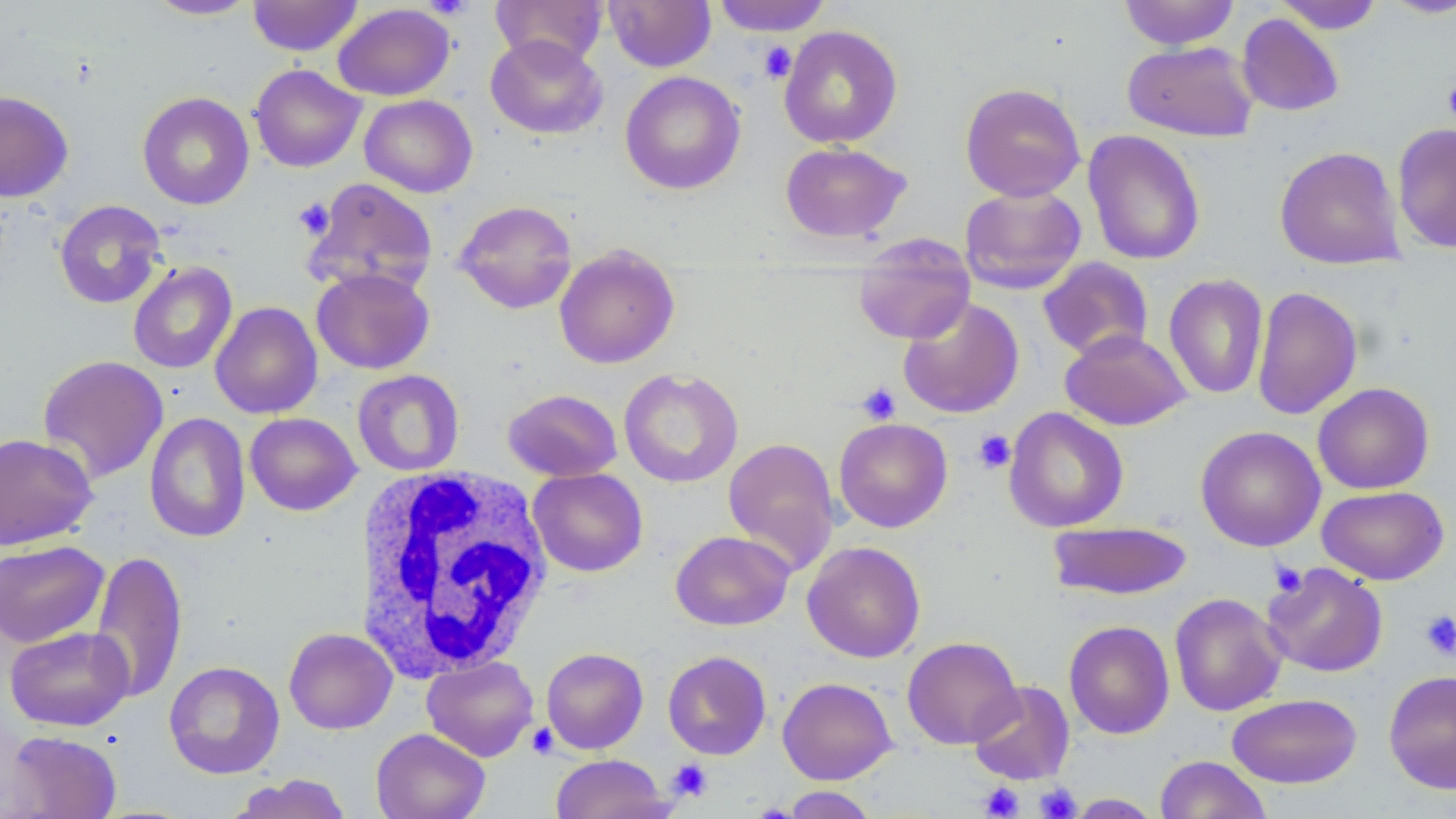

slide_level_diagnosis: negative for blood parasites
preparation: thin blood smear
uninfected_red_blood_cell_locations: 'approximate bounding boxes as named x1/y1/x2/y2 corners in pixels: (x1=145, y1=0, x2=259, y2=20), (x1=248, y1=0, x2=363, y2=55), (x1=490, y1=0, x2=608, y2=68), (x1=604, y1=0, x2=717, y2=72), (x1=712, y1=0, x2=832, y2=36), (x1=1119, y1=0, x2=1239, y2=50), (x1=1379, y1=0, x2=1456, y2=19), (x1=1274, y1=1, x2=1385, y2=34), (x1=333, y1=3, x2=455, y2=101), (x1=1237, y1=13, x2=1344, y2=117), (x1=778, y1=25, x2=903, y2=148), (x1=485, y1=34, x2=607, y2=139), (x1=1122, y1=41, x2=1259, y2=142), (x1=249, y1=64, x2=365, y2=172), (x1=620, y1=71, x2=746, y2=194), (x1=960, y1=82, x2=1086, y2=202), (x1=0, y1=91, x2=74, y2=202), (x1=137, y1=91, x2=255, y2=210), (x1=359, y1=94, x2=478, y2=198), (x1=1391, y1=123, x2=1456, y2=253), (x1=1082, y1=130, x2=1206, y2=266), (x1=780, y1=142, x2=911, y2=243), (x1=1274, y1=146, x2=1405, y2=270), (x1=304, y1=177, x2=438, y2=296), (x1=959, y1=185, x2=1086, y2=295), (x1=54, y1=199, x2=166, y2=308), (x1=454, y1=199, x2=577, y2=314), (x1=852, y1=234, x2=975, y2=344), (x1=554, y1=244, x2=680, y2=369), (x1=1038, y1=257, x2=1154, y2=361), (x1=127, y1=261, x2=237, y2=374), (x1=311, y1=267, x2=435, y2=374), (x1=1164, y1=273, x2=1269, y2=400), (x1=1252, y1=285, x2=1363, y2=421), (x1=898, y1=297, x2=1024, y2=418), (x1=210, y1=301, x2=322, y2=419), (x1=1060, y1=329, x2=1191, y2=431), (x1=37, y1=355, x2=169, y2=484), (x1=619, y1=368, x2=743, y2=488), (x1=352, y1=369, x2=465, y2=476), (x1=1313, y1=382, x2=1435, y2=494), (x1=503, y1=388, x2=622, y2=482), (x1=1004, y1=407, x2=1129, y2=533), (x1=144, y1=411, x2=250, y2=543), (x1=245, y1=412, x2=361, y2=516), (x1=833, y1=417, x2=953, y2=532), (x1=1196, y1=426, x2=1325, y2=551), (x1=0, y1=432, x2=98, y2=550), (x1=722, y1=436, x2=840, y2=575), (x1=528, y1=468, x2=648, y2=577), (x1=1317, y1=485, x2=1449, y2=585), (x1=1048, y1=521, x2=1193, y2=600), (x1=670, y1=530, x2=794, y2=631), (x1=0, y1=540, x2=110, y2=648), (x1=802, y1=541, x2=926, y2=663), (x1=89, y1=549, x2=188, y2=704), (x1=1262, y1=563, x2=1388, y2=678), (x1=1169, y1=593, x2=1288, y2=717), (x1=1063, y1=620, x2=1175, y2=739), (x1=5, y1=626, x2=135, y2=731), (x1=283, y1=628, x2=398, y2=734), (x1=901, y1=636, x2=1022, y2=749), (x1=541, y1=647, x2=648, y2=754), (x1=662, y1=650, x2=771, y2=760), (x1=422, y1=656, x2=539, y2=761), (x1=163, y1=661, x2=285, y2=779), (x1=1384, y1=670, x2=1456, y2=794), (x1=778, y1=677, x2=897, y2=784), (x1=968, y1=680, x2=1075, y2=786), (x1=1227, y1=693, x2=1362, y2=788), (x1=371, y1=728, x2=490, y2=819), (x1=4, y1=730, x2=122, y2=818), (x1=550, y1=754, x2=672, y2=819), (x1=1155, y1=755, x2=1272, y2=819), (x1=227, y1=774, x2=353, y2=819), (x1=779, y1=786, x2=877, y2=818), (x1=1063, y1=794, x2=1164, y2=818)'
magnification: 1000x
white_blood_cell_locations: 'approximate bounding boxes as named x1/y1/x2/y2 corners in pixels: (x1=354, y1=466, x2=554, y2=682)'
stain: May-Grünwald-Giemsa
image_size: 1456×819 pixels
field_of_view: one of a larger specimen
platelet_locations: 'approximate bounding boxes as named x1/y1/x2/y2 corners in pixels: (x1=423, y1=0, x2=474, y2=20), (x1=757, y1=41, x2=797, y2=84), (x1=1443, y1=75, x2=1456, y2=129), (x1=293, y1=197, x2=335, y2=239), (x1=856, y1=382, x2=901, y2=425), (x1=972, y1=429, x2=1016, y2=474), (x1=1269, y1=561, x2=1307, y2=598), (x1=1419, y1=609, x2=1456, y2=660), (x1=526, y1=723, x2=558, y2=759), (x1=667, y1=759, x2=713, y2=802), (x1=979, y1=782, x2=1024, y2=818), (x1=1036, y1=783, x2=1081, y2=818)'
modality: optical microscopy